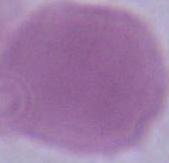
modality = micrograph
identification = erythrocyte
magnification = 1000x